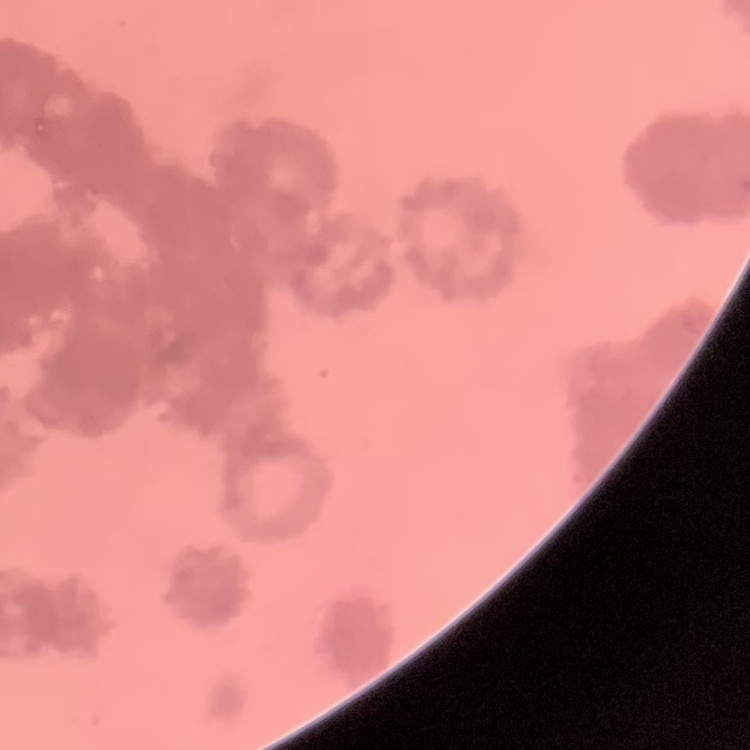
Summary:
  - Red blood cell morphology: rouleaux formation
  - Preparation: thin blood film
  - Image type: one tile cut from a larger photomicrograph
  - Stain: Field's or Giemsa